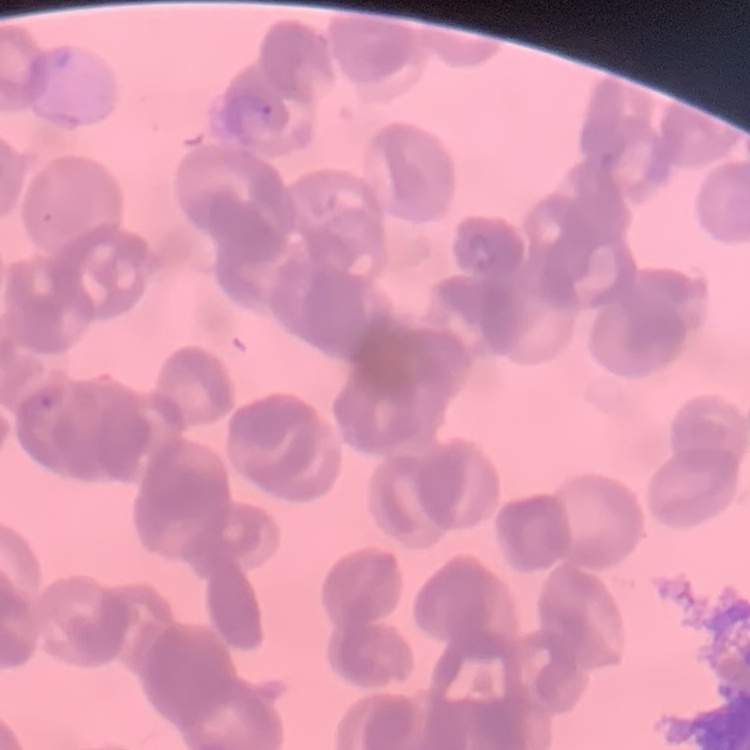
The red blood cells exhibit rouleaux formation. Square crop of a larger photomicrograph. Stained with either Field's or Giemsa. Thin blood film.